Assess the morphology of the red blood cells.
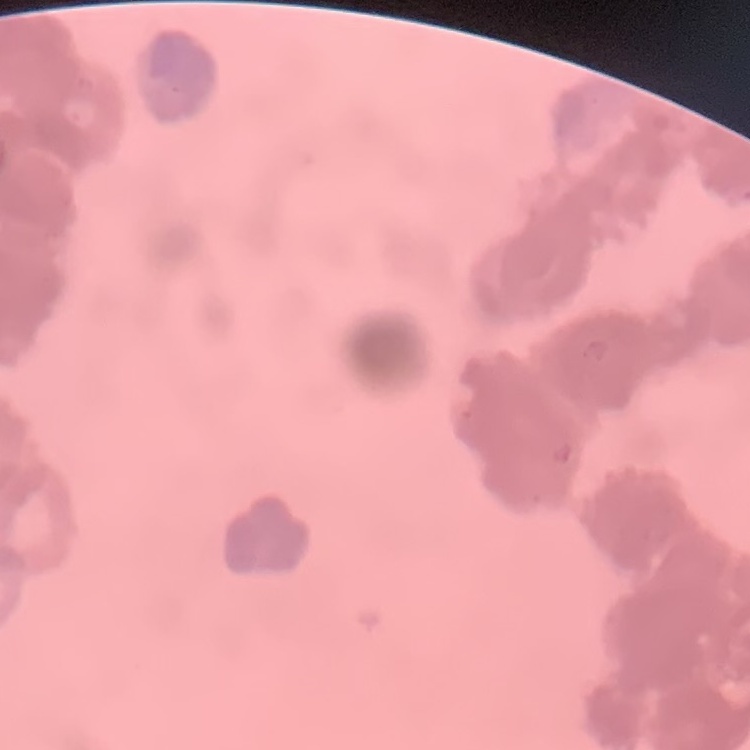

They show rouleaux formation.

image type = one tile cut from a larger photomicrograph
preparation = thin blood smear
stain = Field's or Giemsa